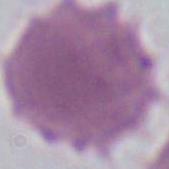

magnification = 1000x
modality = photomicrograph
identification = erythrocyte